State which parasite is depicted.
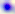
Toxoplasma gondii.

Summary:
  - Modality: photomicrograph
  - Magnification: 400x